Name the parasite shown.
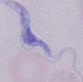
A trypanosome.

Micrograph. 1000x magnification.